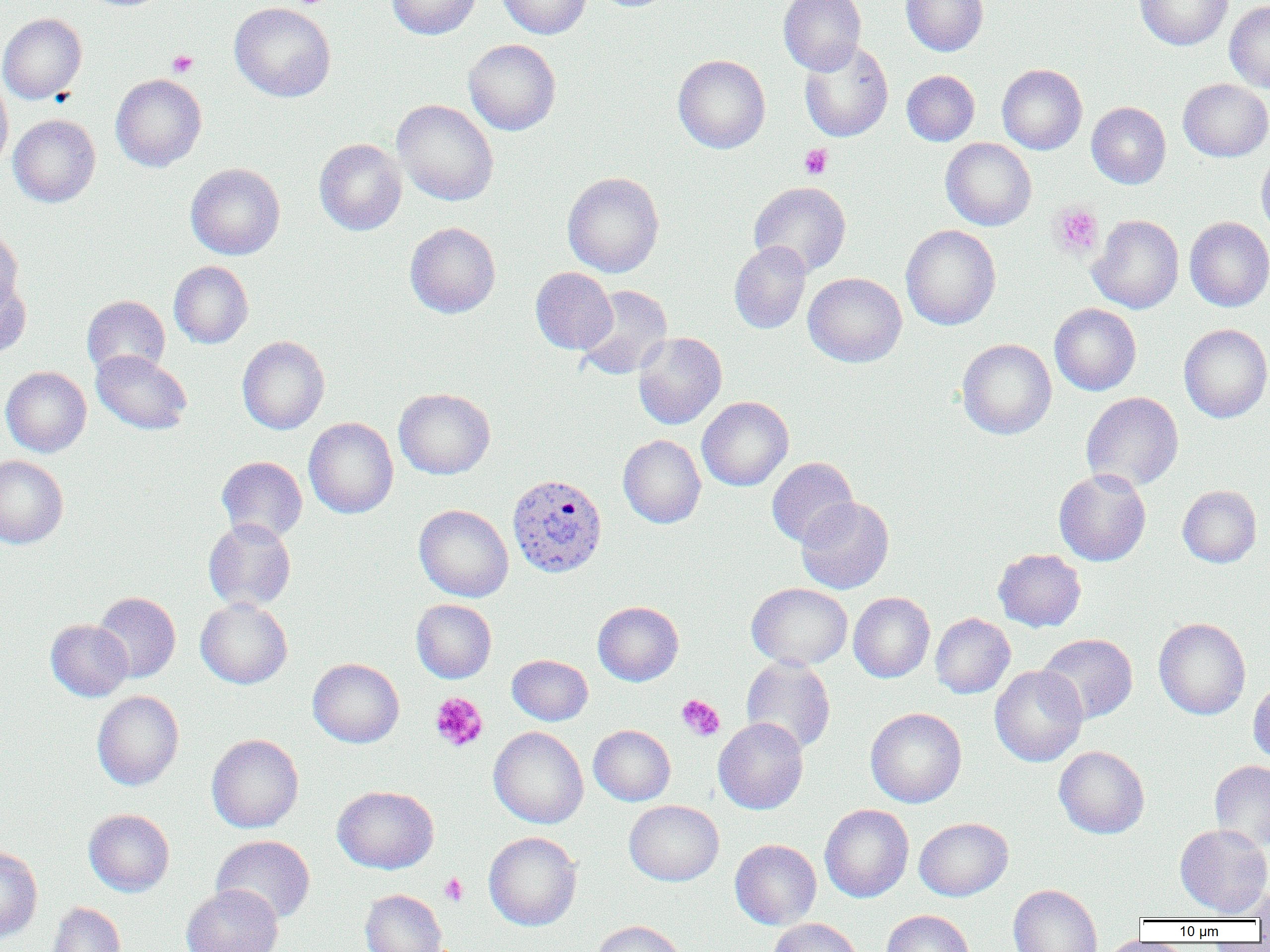
Summary:
  - Coordinate format: approximate bounding boxes as named x1/y1/x2/y2 corners in pixels
  - Uninfected red blood cell locations: (x1=386, y1=0, x2=480, y2=40), (x1=496, y1=0, x2=592, y2=39), (x1=778, y1=0, x2=866, y2=75), (x1=901, y1=0, x2=988, y2=56), (x1=1135, y1=0, x2=1233, y2=50), (x1=1225, y1=1, x2=1270, y2=93), (x1=229, y1=2, x2=336, y2=102), (x1=0, y1=13, x2=87, y2=104), (x1=463, y1=39, x2=561, y2=135), (x1=798, y1=40, x2=893, y2=141), (x1=673, y1=54, x2=770, y2=154), (x1=997, y1=64, x2=1087, y2=154), (x1=902, y1=70, x2=980, y2=146), (x1=110, y1=73, x2=206, y2=172), (x1=0, y1=75, x2=13, y2=173), (x1=1178, y1=79, x2=1270, y2=161), (x1=392, y1=99, x2=498, y2=206), (x1=1086, y1=102, x2=1171, y2=189), (x1=9, y1=114, x2=100, y2=206), (x1=314, y1=138, x2=407, y2=236), (x1=941, y1=138, x2=1037, y2=230), (x1=1256, y1=150, x2=1270, y2=242), (x1=186, y1=163, x2=285, y2=259), (x1=562, y1=172, x2=664, y2=277), (x1=748, y1=181, x2=851, y2=277), (x1=1087, y1=214, x2=1184, y2=314), (x1=1185, y1=217, x2=1270, y2=311), (x1=405, y1=222, x2=501, y2=318), (x1=900, y1=225, x2=1001, y2=330), (x1=0, y1=227, x2=24, y2=312), (x1=729, y1=241, x2=811, y2=334), (x1=169, y1=261, x2=253, y2=348), (x1=531, y1=267, x2=617, y2=354), (x1=803, y1=272, x2=906, y2=367), (x1=0, y1=275, x2=31, y2=358), (x1=575, y1=284, x2=673, y2=380), (x1=82, y1=295, x2=170, y2=377), (x1=1049, y1=303, x2=1141, y2=395), (x1=1179, y1=323, x2=1270, y2=423), (x1=633, y1=332, x2=727, y2=429), (x1=237, y1=336, x2=329, y2=434), (x1=957, y1=338, x2=1057, y2=440), (x1=92, y1=349, x2=191, y2=434), (x1=1, y1=366, x2=91, y2=457), (x1=393, y1=388, x2=495, y2=479), (x1=1081, y1=392, x2=1183, y2=492), (x1=697, y1=396, x2=793, y2=491), (x1=304, y1=417, x2=398, y2=519), (x1=618, y1=434, x2=706, y2=528), (x1=0, y1=455, x2=68, y2=549), (x1=217, y1=456, x2=307, y2=543), (x1=766, y1=457, x2=858, y2=548), (x1=1054, y1=468, x2=1151, y2=566), (x1=1178, y1=485, x2=1262, y2=567), (x1=796, y1=496, x2=894, y2=594), (x1=414, y1=504, x2=513, y2=602), (x1=203, y1=518, x2=296, y2=611), (x1=993, y1=549, x2=1086, y2=632), (x1=746, y1=583, x2=852, y2=670), (x1=93, y1=592, x2=180, y2=683), (x1=848, y1=592, x2=934, y2=683), (x1=195, y1=598, x2=293, y2=689), (x1=411, y1=599, x2=497, y2=683), (x1=593, y1=601, x2=684, y2=686), (x1=930, y1=613, x2=1015, y2=699), (x1=1153, y1=618, x2=1251, y2=720), (x1=45, y1=619, x2=132, y2=701), (x1=1038, y1=633, x2=1138, y2=724), (x1=507, y1=654, x2=593, y2=725), (x1=741, y1=656, x2=835, y2=754), (x1=308, y1=658, x2=404, y2=748), (x1=990, y1=664, x2=1087, y2=767), (x1=1248, y1=679, x2=1270, y2=765), (x1=92, y1=690, x2=184, y2=791), (x1=866, y1=707, x2=967, y2=807), (x1=713, y1=717, x2=808, y2=814), (x1=588, y1=724, x2=675, y2=806), (x1=489, y1=726, x2=588, y2=828), (x1=206, y1=733, x2=304, y2=833), (x1=1054, y1=746, x2=1149, y2=838), (x1=1209, y1=760, x2=1270, y2=851), (x1=332, y1=785, x2=439, y2=874), (x1=624, y1=800, x2=723, y2=886), (x1=820, y1=804, x2=914, y2=903), (x1=84, y1=809, x2=174, y2=896), (x1=914, y1=817, x2=1013, y2=901), (x1=1175, y1=823, x2=1270, y2=917), (x1=483, y1=831, x2=582, y2=931), (x1=211, y1=835, x2=315, y2=924), (x1=730, y1=839, x2=821, y2=929), (x1=0, y1=846, x2=43, y2=943), (x1=182, y1=884, x2=282, y2=952), (x1=1009, y1=884, x2=1102, y2=952), (x1=1252, y1=885, x2=1270, y2=923), (x1=360, y1=889, x2=447, y2=952), (x1=47, y1=902, x2=125, y2=952), (x1=882, y1=909, x2=974, y2=952), (x1=768, y1=918, x2=864, y2=952), (x1=589, y1=920, x2=687, y2=952), (x1=1099, y1=937, x2=1176, y2=952)
  - Plasmodium vivax-infected red blood cell locations: (x1=507, y1=473, x2=607, y2=578)
  - Platelet locations: (x1=286, y1=0, x2=334, y2=9), (x1=166, y1=50, x2=198, y2=77), (x1=799, y1=144, x2=832, y2=179), (x1=1050, y1=202, x2=1104, y2=259), (x1=430, y1=692, x2=488, y2=752), (x1=676, y1=694, x2=725, y2=741), (x1=439, y1=873, x2=468, y2=906)
  - Slide-level diagnosis: Plasmodium vivax
  - Magnification: 1000x
  - Field of view: one of a larger specimen
  - Preparation: thin blood smear
  - Modality: light microscopy
  - Image size: 1270×952 pixels